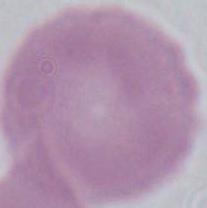
A red blood cell is shown. Photomicrograph. Captured at 1000x magnification.